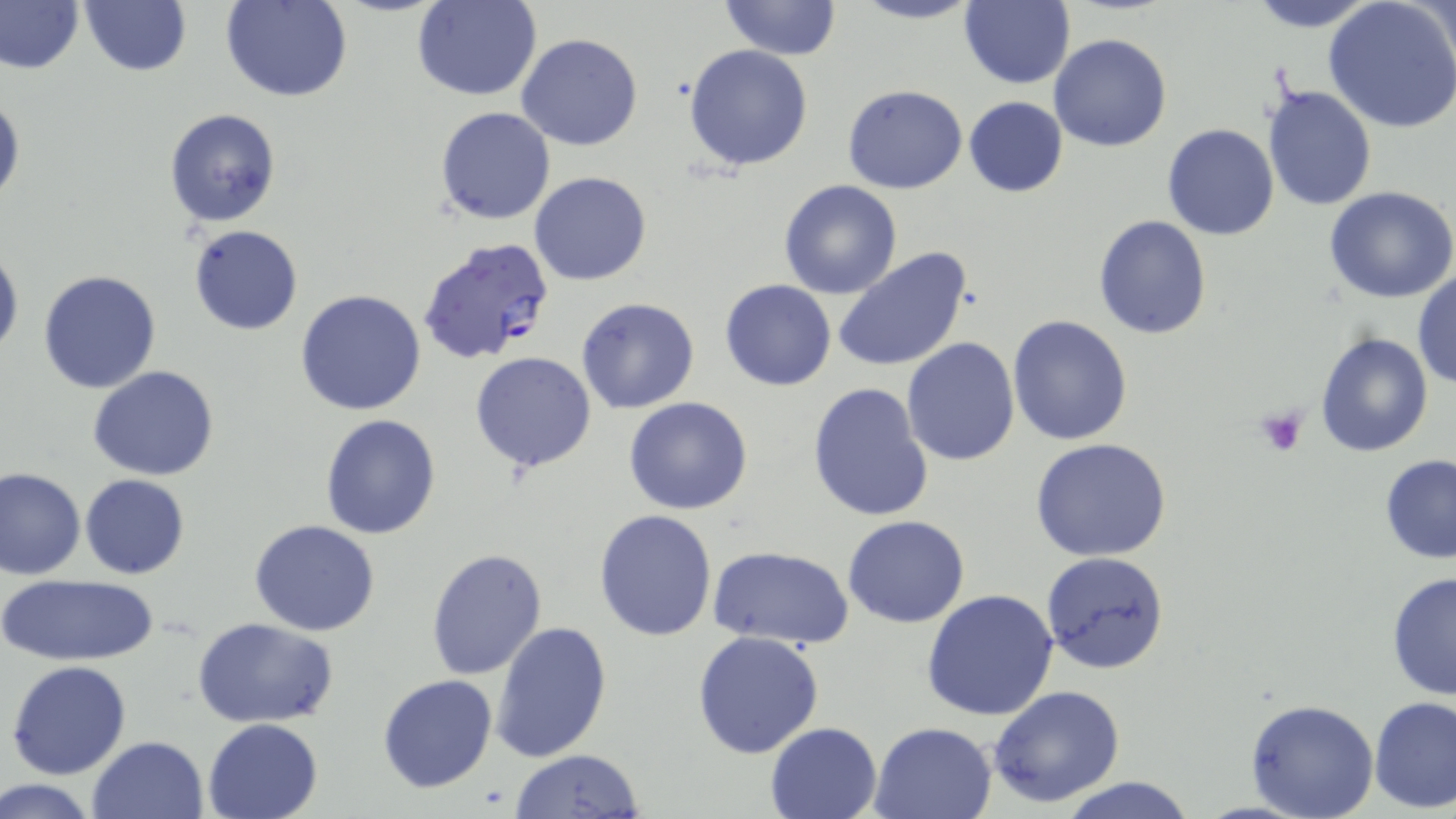 Approximate bounding boxes as (x1, y1, x2, y2) in pixels. Platelet locations: (1254, 406, 1308, 457). Uninfected red blood cell locations: (222, 0, 350, 102), (414, 0, 542, 101), (718, 0, 842, 59), (848, 0, 982, 25), (958, 0, 1074, 89), (1245, 0, 1378, 31), (1, 1, 82, 75), (1324, 1, 1456, 136), (78, 2, 192, 77), (515, 33, 643, 152), (1048, 33, 1173, 152), (684, 43, 815, 173), (842, 85, 969, 194), (1262, 85, 1376, 211), (1, 90, 25, 206), (964, 96, 1067, 197), (1173, 104, 1373, 226), (434, 106, 556, 224), (164, 107, 282, 230), (1162, 123, 1281, 241), (530, 172, 652, 287), (778, 180, 903, 299), (1324, 186, 1456, 303), (1093, 216, 1212, 339), (189, 225, 303, 336), (0, 240, 22, 363), (834, 248, 972, 374), (39, 269, 161, 394), (1413, 269, 1456, 390), (718, 279, 836, 390), (294, 288, 427, 415), (576, 297, 699, 415), (1007, 315, 1132, 446), (1315, 332, 1434, 457), (902, 336, 1019, 467), (469, 351, 597, 474), (88, 366, 220, 480), (805, 382, 934, 524), (623, 397, 754, 515), (319, 413, 443, 539), (1031, 438, 1172, 561), (1378, 454, 1456, 564), (0, 468, 85, 581), (79, 474, 189, 578), (593, 509, 718, 642), (842, 515, 970, 627), (249, 519, 380, 637), (709, 545, 855, 649), (425, 549, 548, 680), (1040, 552, 1170, 674), (1387, 570, 1456, 704), (0, 573, 161, 666), (921, 588, 1058, 721), (194, 617, 338, 728), (491, 619, 613, 762), (691, 630, 825, 759), (6, 661, 132, 780), (376, 674, 498, 794), (987, 686, 1127, 808), (1368, 695, 1456, 811), (1245, 698, 1378, 819), (202, 717, 326, 819), (869, 720, 997, 819), (764, 721, 884, 818), (87, 734, 210, 819), (509, 748, 645, 818), (1055, 777, 1201, 818), (0, 779, 98, 817). Plasmodium falciparum-infected red blood cell locations: (418, 238, 555, 366). Slide-level diagnosis: Plasmodium falciparum. 1000x magnification. Thin blood film. Image is 1456×819 pixels. Light microscopy. One field of a larger specimen. May-Grünwald-Giemsa-stained preparation.